Classify this cell by malaria status.
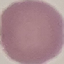

It is uninfected.

Summary:
  - Preparation: thin smear
  - Image type: cell patch, automatically extracted from a larger field of view and resized to 64 × 64 pixels
  - Capture: smartphone through the microscope eyepiece
  - Stain: Giemsa